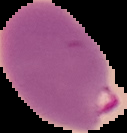
image size = 127×133 pixels
preparation = thin blood film
image type = segmented cell region on a black background
result = Plasmodium parasites identified